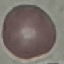 Malaria status: uninfected. Photographed with a smartphone camera at the microscope eyepiece. Thin smear of blood. Giemsa stain. Cell patch, automatically extracted from a larger field of view and resized to 64 × 64 pixels.